Assess the morphology of the erythrocytes.
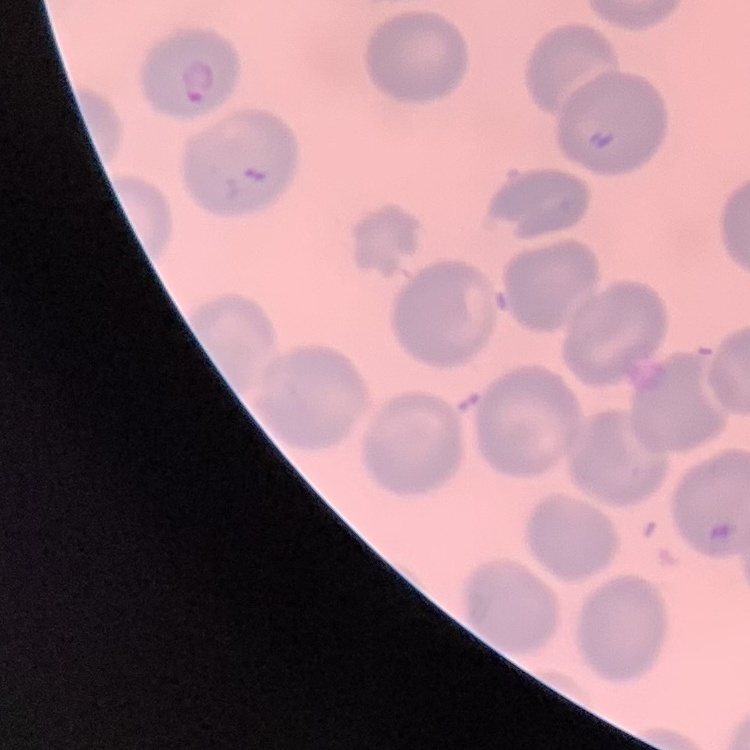

No rouleaux formation.

image_type: square crop of a larger photomicrograph
preparation: thin blood film
stain: Field's or Giemsa